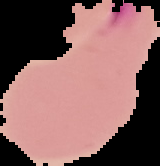
image type = segmented cell region on a black background
image size = 160×166 pixels
preparation = thin blood smear
result = Plasmodium parasites detected